Report the malaria status of this cell.
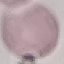
Uninfected.

Photographed with a smartphone camera at the microscope eyepiece. Automatically extracted cell patch, resized to 64 × 64 pixels. Thin blood smear. Giemsa-stained preparation.